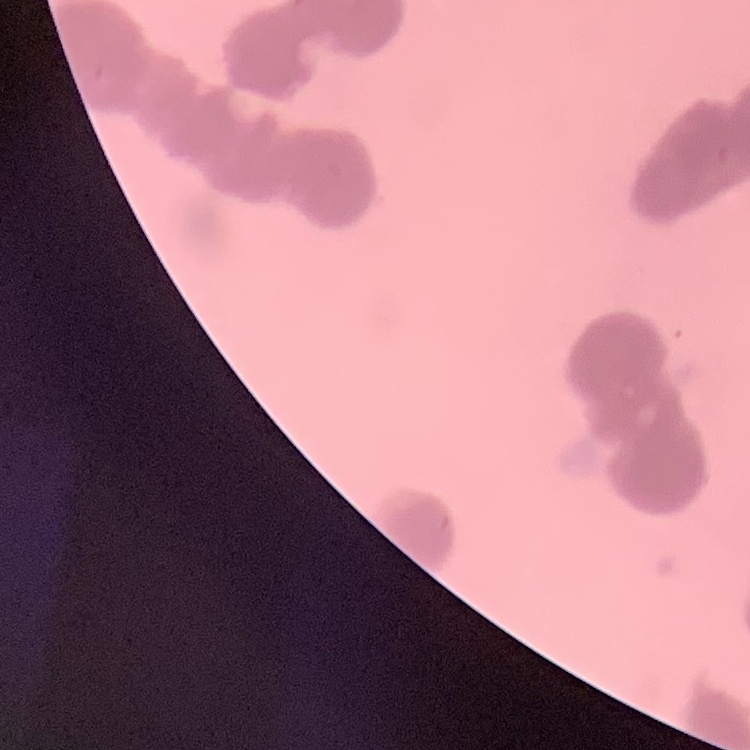

erythrocyte morphology = rouleaux formation
image type = one tile cut from a larger photomicrograph
preparation = thin blood smear
stain = Field's or Giemsa